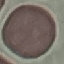
{
  "result": "no malaria parasites seen",
  "image_type": "automatically extracted cell patch, resized to 64 × 64 pixels",
  "stain": "Giemsa",
  "preparation": "thin blood smear",
  "capture": "smartphone through the microscope eyepiece"
}